Evaluate for malaria.
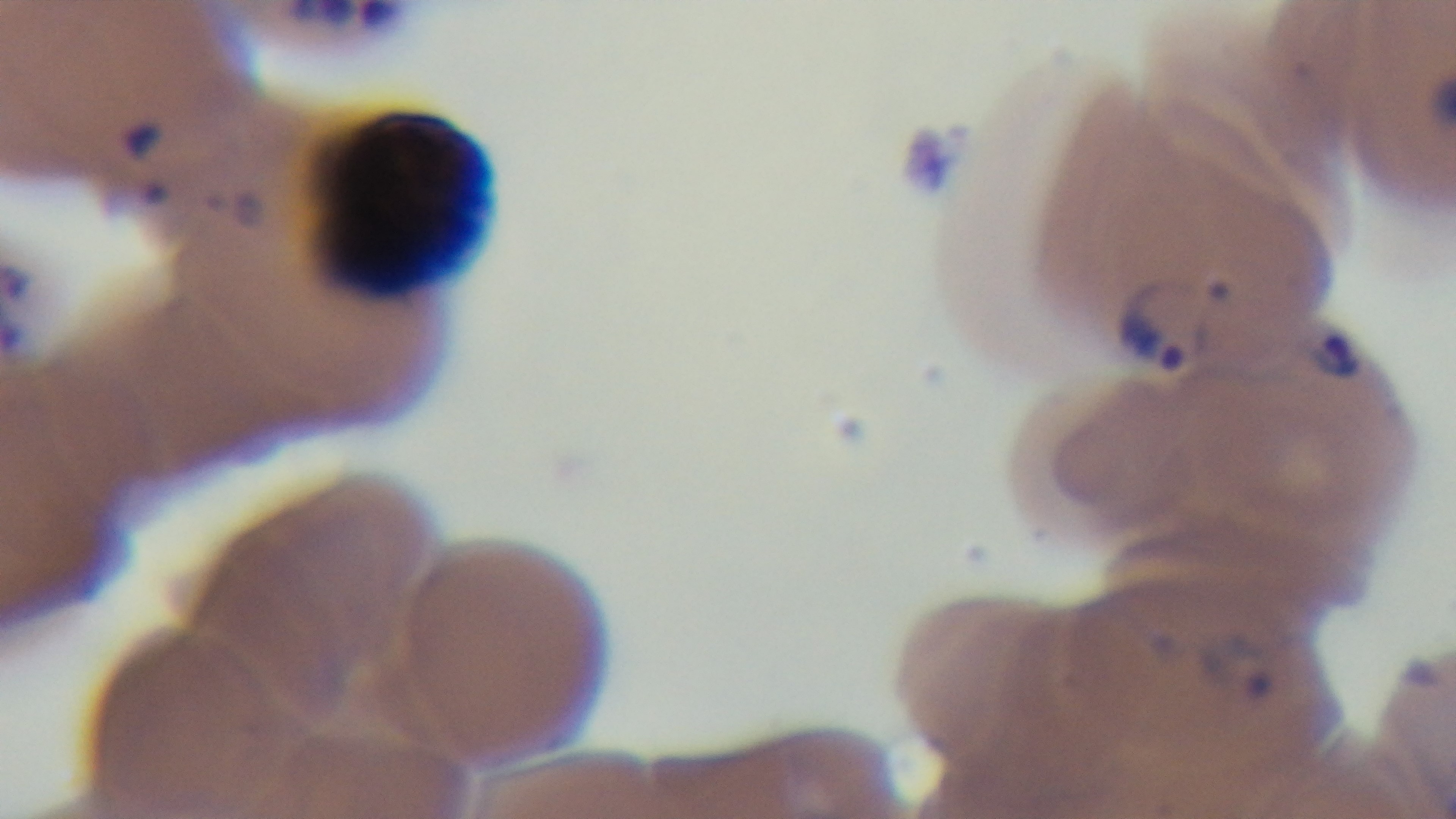
Infected.

{
  "field_of_view": "one from the slide",
  "capture": "mounted 4K digital camera",
  "stain": "Giemsa",
  "objective": "100x oil immersion",
  "preparation": "thin blood film",
  "modality": "light microscopy"
}